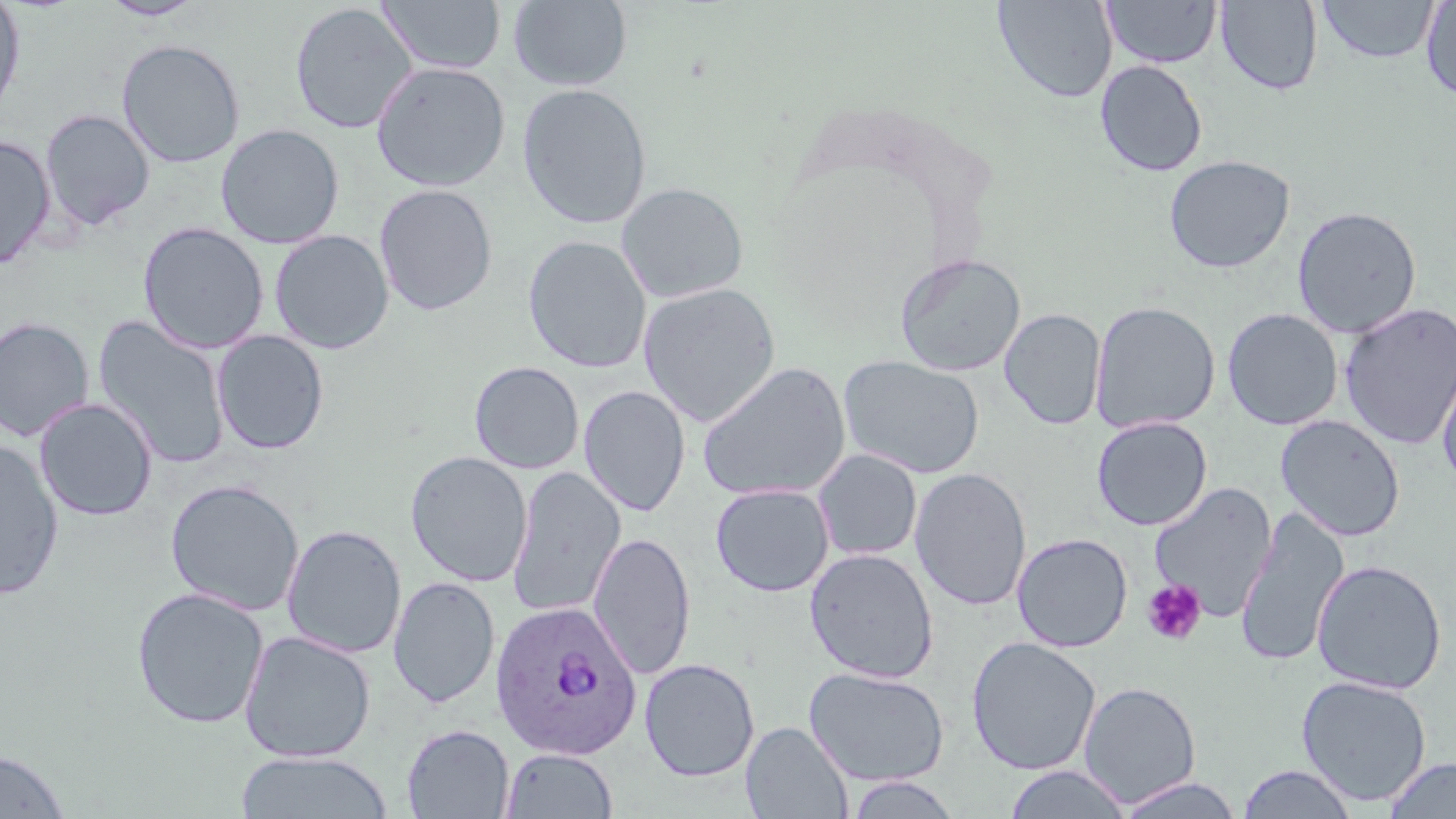 Approximate bounding boxes as named x1/y1/x2/y2 corners in pixels. Plasmodium ovale-infected red blood cell locations: (x1=490, y1=600, x2=642, y2=759). Platelet locations: (x1=1141, y1=579, x2=1207, y2=646). Uninfected red blood cell locations: (x1=0, y1=0, x2=26, y2=121), (x1=378, y1=0, x2=505, y2=75), (x1=508, y1=0, x2=633, y2=92), (x1=992, y1=0, x2=1117, y2=104), (x1=1102, y1=0, x2=1222, y2=68), (x1=98, y1=1, x2=207, y2=21), (x1=1214, y1=1, x2=1323, y2=96), (x1=1317, y1=1, x2=1439, y2=64), (x1=1420, y1=1, x2=1456, y2=104), (x1=289, y1=2, x2=417, y2=134), (x1=116, y1=39, x2=246, y2=168), (x1=371, y1=60, x2=511, y2=192), (x1=1095, y1=60, x2=1208, y2=177), (x1=517, y1=83, x2=652, y2=230), (x1=40, y1=108, x2=155, y2=231), (x1=215, y1=124, x2=344, y2=249), (x1=0, y1=135, x2=57, y2=269), (x1=1164, y1=154, x2=1296, y2=274), (x1=616, y1=182, x2=749, y2=304), (x1=374, y1=184, x2=498, y2=316), (x1=1292, y1=206, x2=1422, y2=339), (x1=138, y1=222, x2=269, y2=354), (x1=269, y1=229, x2=394, y2=355), (x1=523, y1=235, x2=652, y2=374), (x1=894, y1=253, x2=1026, y2=376), (x1=638, y1=283, x2=781, y2=426), (x1=1089, y1=301, x2=1220, y2=434), (x1=1339, y1=301, x2=1456, y2=450), (x1=999, y1=308, x2=1106, y2=430), (x1=1222, y1=308, x2=1343, y2=430), (x1=93, y1=314, x2=231, y2=469), (x1=0, y1=316, x2=95, y2=442), (x1=211, y1=330, x2=329, y2=454), (x1=1436, y1=352, x2=1456, y2=492), (x1=838, y1=354, x2=986, y2=479), (x1=469, y1=361, x2=584, y2=474), (x1=697, y1=361, x2=852, y2=503), (x1=578, y1=385, x2=690, y2=517), (x1=34, y1=397, x2=158, y2=522), (x1=1275, y1=414, x2=1406, y2=542), (x1=1091, y1=416, x2=1212, y2=531), (x1=0, y1=440, x2=64, y2=600), (x1=813, y1=449, x2=923, y2=561), (x1=405, y1=451, x2=533, y2=587), (x1=507, y1=466, x2=626, y2=619), (x1=910, y1=467, x2=1032, y2=612), (x1=165, y1=479, x2=305, y2=616), (x1=1149, y1=482, x2=1278, y2=622), (x1=710, y1=483, x2=834, y2=597), (x1=1234, y1=507, x2=1349, y2=668), (x1=282, y1=524, x2=406, y2=658), (x1=589, y1=531, x2=695, y2=679), (x1=1012, y1=533, x2=1132, y2=652), (x1=804, y1=548, x2=939, y2=683), (x1=1311, y1=559, x2=1447, y2=694), (x1=388, y1=576, x2=500, y2=708), (x1=131, y1=587, x2=269, y2=729), (x1=239, y1=630, x2=376, y2=763), (x1=966, y1=636, x2=1102, y2=776), (x1=639, y1=658, x2=760, y2=781), (x1=803, y1=665, x2=951, y2=786), (x1=1296, y1=675, x2=1432, y2=806), (x1=1078, y1=681, x2=1202, y2=807), (x1=742, y1=721, x2=852, y2=818), (x1=401, y1=723, x2=514, y2=818), (x1=501, y1=747, x2=618, y2=818), (x1=0, y1=749, x2=70, y2=818), (x1=234, y1=751, x2=393, y2=818), (x1=1382, y1=757, x2=1456, y2=818), (x1=1003, y1=765, x2=1133, y2=819), (x1=1237, y1=765, x2=1359, y2=819), (x1=846, y1=774, x2=963, y2=818), (x1=1111, y1=776, x2=1247, y2=818). Slide-level diagnosis: Plasmodium ovale. Image is 1456×819 pixels. Single field of view. Optical microscopy. 1000x magnification. May-Grünwald-Giemsa stain. Thin blood film.